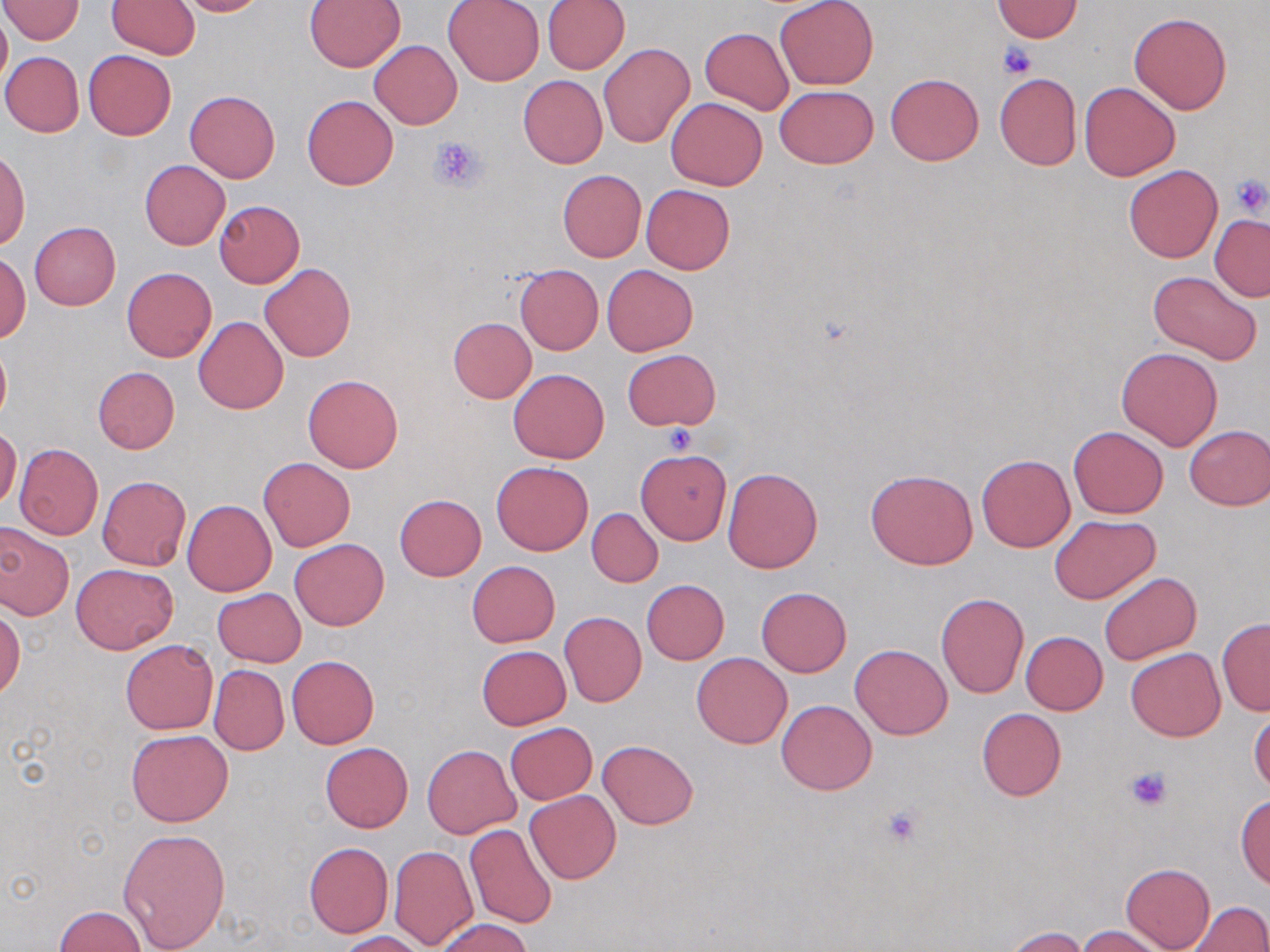 Approximate bounding boxes as (x1,y1)-(x2,y2) corner pairs in pixels. Platelet locations: (998,42)-(1037,80), (429,135)-(485,192), (1229,173)-(1267,218), (660,422)-(696,456), (1125,766)-(1173,812), (880,803)-(924,845). Uninfected red blood cell locations: (1,0)-(84,44), (173,0)-(267,17), (442,0)-(544,86), (542,0)-(630,74), (775,0)-(878,89), (107,1)-(200,58), (305,1)-(406,72), (990,1)-(1084,41), (0,11)-(11,90), (1129,11)-(1233,114), (700,27)-(794,115), (370,41)-(462,128), (599,43)-(693,146), (84,50)-(176,139), (1,52)-(84,137), (886,73)-(983,165), (994,73)-(1082,170), (518,75)-(607,168), (1080,81)-(1181,181), (776,86)-(877,168), (183,89)-(280,183), (302,95)-(398,190), (666,97)-(767,191), (0,151)-(29,249), (140,160)-(231,250), (1123,165)-(1222,263), (557,170)-(647,262), (641,184)-(734,274), (214,200)-(305,287), (1210,214)-(1270,302), (29,223)-(121,310), (1,251)-(30,343), (260,263)-(355,362), (514,264)-(603,355), (601,264)-(699,356), (122,267)-(216,361), (1148,270)-(1263,365), (194,316)-(288,415), (447,317)-(537,404), (0,337)-(11,427), (1116,346)-(1224,451), (622,349)-(720,431), (92,366)-(179,453), (508,368)-(609,462), (303,374)-(403,473), (1184,425)-(1269,511), (0,427)-(21,510), (1068,427)-(1169,518), (14,443)-(104,540), (636,448)-(732,544), (977,454)-(1074,551), (259,458)-(355,551), (492,460)-(592,555), (722,467)-(822,572), (865,469)-(978,570), (98,475)-(190,571), (393,494)-(487,580), (181,498)-(277,596), (586,508)-(662,587), (1050,516)-(1161,604), (0,522)-(74,620), (289,538)-(390,630), (466,561)-(560,647), (71,562)-(177,654), (1098,572)-(1202,664), (641,579)-(729,664), (757,587)-(851,676), (212,588)-(305,667), (936,591)-(1029,698), (0,608)-(23,700), (559,612)-(647,707), (1217,617)-(1270,716), (1020,631)-(1108,714), (119,639)-(217,734), (851,644)-(951,739), (475,645)-(572,730), (1125,648)-(1225,741), (693,652)-(792,749), (287,655)-(379,748), (209,664)-(289,755), (776,700)-(876,795), (1249,706)-(1270,796), (976,708)-(1066,801), (505,722)-(596,804), (125,729)-(233,827), (599,739)-(698,829), (320,743)-(413,833), (422,744)-(521,838), (525,790)-(621,884), (1235,793)-(1270,891), (463,825)-(557,928), (119,828)-(230,950), (304,842)-(394,937), (389,845)-(477,949), (1120,863)-(1216,952), (1189,902)-(1269,951), (55,906)-(148,951), (432,917)-(535,951), (1077,925)-(1170,952), (1003,926)-(1093,952), (335,931)-(430,952). Slide-level diagnosis: negative for blood parasites. 1000x magnification. Light microscopy. May-Grünwald-Giemsa-stained preparation. Thin blood film. Single field of view. Image is 1270×952 pixels.